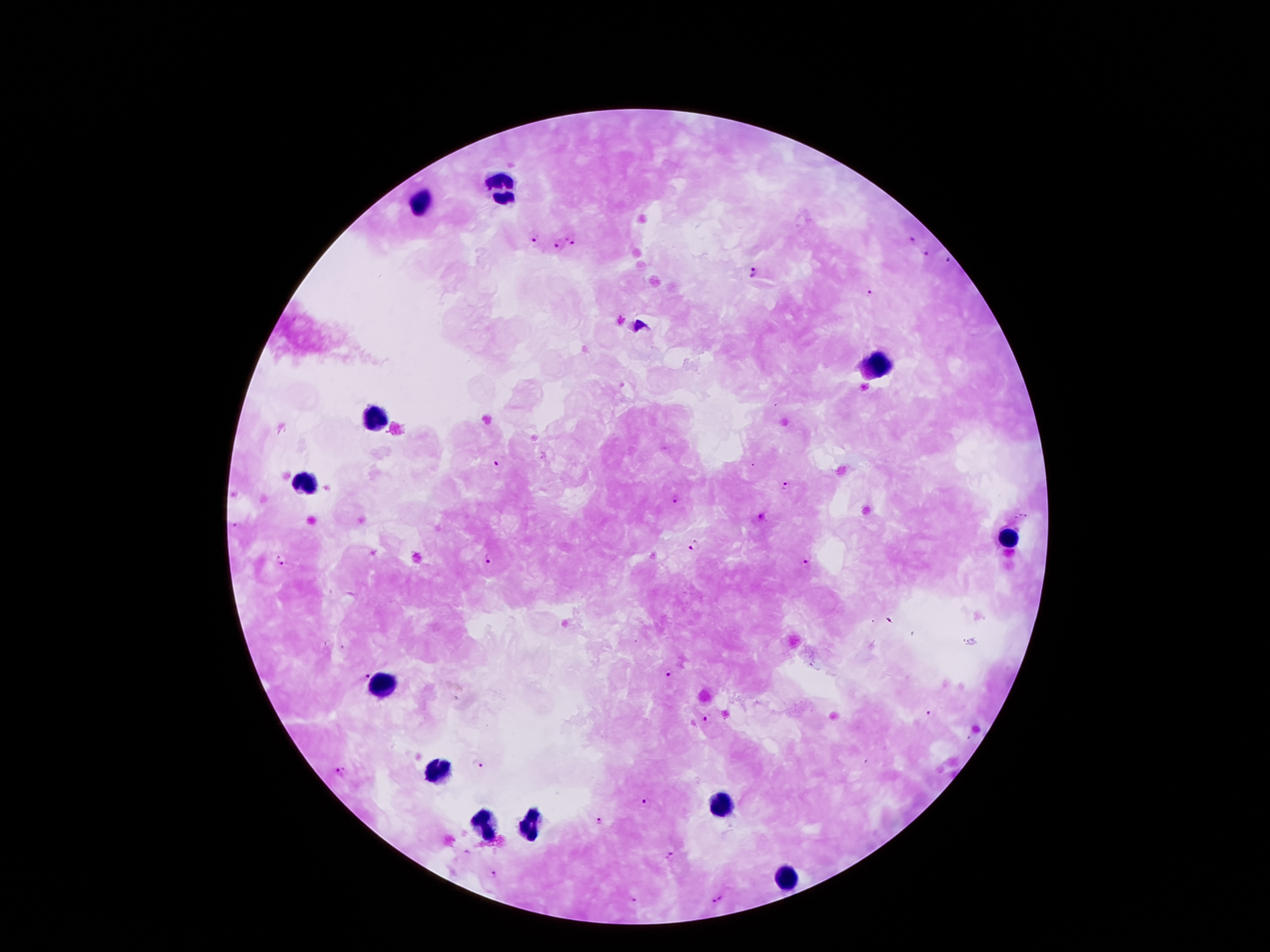
Approximate centers as (x, y) in pixels.
Summary:
  - Leukocyte locations: (503, 188), (421, 203), (876, 367), (372, 416), (306, 485), (1005, 539), (384, 684), (437, 772), (722, 803), (527, 826), (482, 828), (788, 879)
  - Plasmodium parasite locations: (533, 237), (574, 237), (916, 239), (558, 245), (926, 255), (949, 259), (753, 270), (870, 292), (638, 325), (499, 460), (785, 486), (676, 497), (762, 517), (236, 526), (694, 544), (489, 557), (286, 559), (809, 559), (365, 672), (669, 674), (930, 714), (708, 718), (479, 763), (342, 770), (646, 800), (599, 820), (669, 857), (494, 873), (634, 901), (719, 901)
  - Patient malaria status: infected with Plasmodium falciparum
  - Magnification: 100x
  - Field of view: single
  - Preparation: thick blood smear
  - Image size: 1270×952 pixels
  - Capture: smartphone camera through the microscope eyepiece
  - Stain: Giemsa